Classify this cell by malaria status.
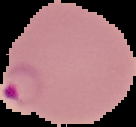
It is parasitized.

The area outside the segmented cell region is set to black. Image is 136×127 pixels. From a thin blood smear.